Outline each Plasmodium malariae-infected red blood cell.
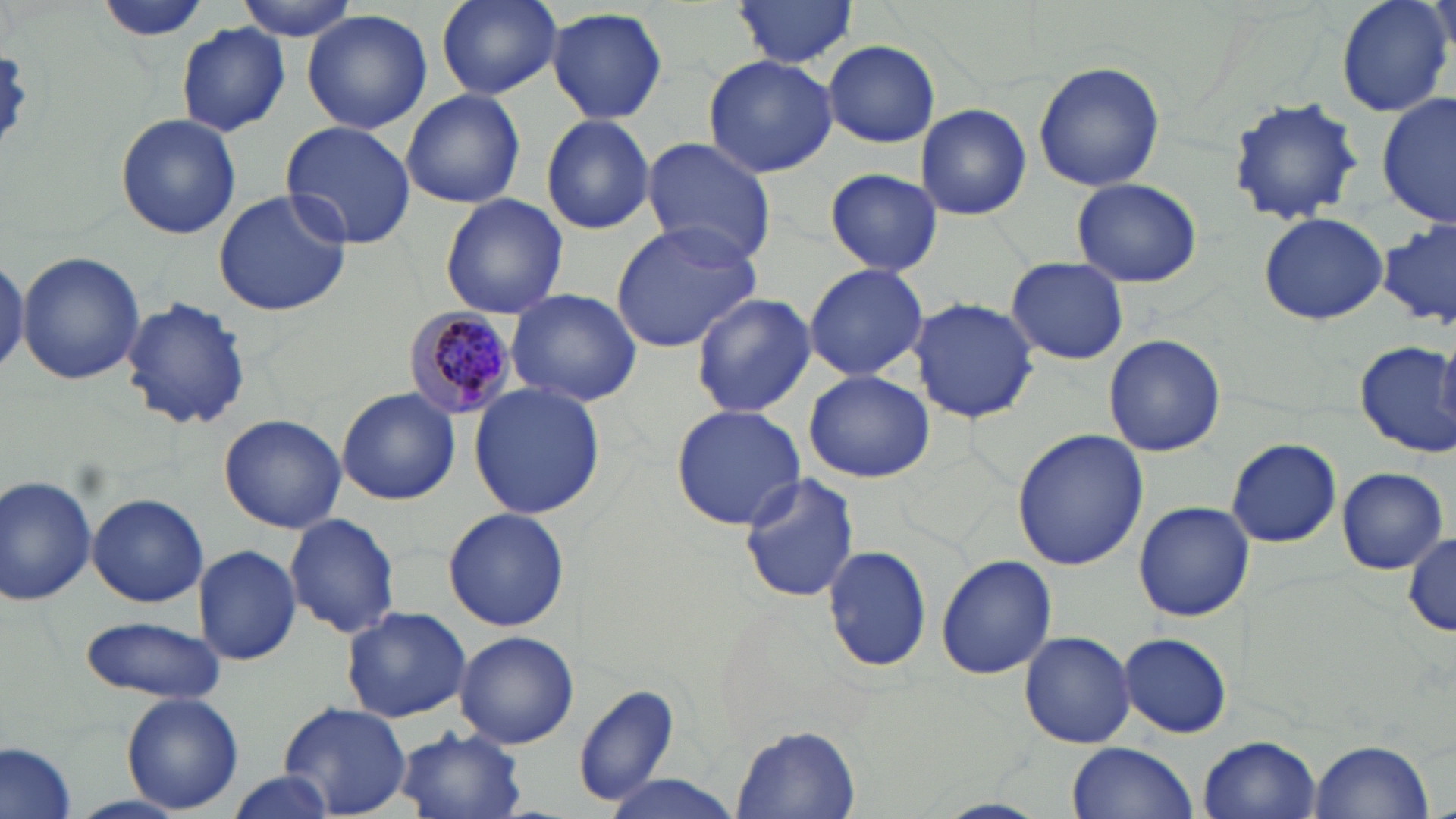

Approximate bounding boxes as named x1/y1/x2/y2 corners in pixels.
Plasmodium malariae-infected red blood cells: (x1=401, y1=304, x2=523, y2=419).

Summary:
  - Uninfected red blood cell locations: (x1=95, y1=0, x2=212, y2=46), (x1=237, y1=0, x2=363, y2=40), (x1=434, y1=0, x2=562, y2=100), (x1=732, y1=0, x2=860, y2=70), (x1=1334, y1=0, x2=1455, y2=119), (x1=547, y1=7, x2=668, y2=125), (x1=301, y1=9, x2=433, y2=135), (x1=176, y1=22, x2=292, y2=136), (x1=823, y1=40, x2=940, y2=147), (x1=701, y1=54, x2=839, y2=177), (x1=1033, y1=60, x2=1166, y2=192), (x1=400, y1=89, x2=525, y2=209), (x1=1378, y1=94, x2=1453, y2=227), (x1=1225, y1=97, x2=1367, y2=225), (x1=916, y1=104, x2=1031, y2=221), (x1=115, y1=113, x2=241, y2=240), (x1=540, y1=114, x2=657, y2=235), (x1=281, y1=120, x2=417, y2=248), (x1=640, y1=138, x2=776, y2=265), (x1=825, y1=167, x2=943, y2=275), (x1=1070, y1=177, x2=1204, y2=289), (x1=213, y1=188, x2=354, y2=317), (x1=439, y1=194, x2=567, y2=319), (x1=1258, y1=212, x2=1389, y2=325), (x1=608, y1=221, x2=764, y2=354), (x1=1376, y1=221, x2=1456, y2=330), (x1=17, y1=251, x2=146, y2=386), (x1=0, y1=253, x2=27, y2=377), (x1=1005, y1=257, x2=1130, y2=365), (x1=803, y1=263, x2=928, y2=383), (x1=505, y1=286, x2=645, y2=407), (x1=691, y1=293, x2=815, y2=420), (x1=120, y1=296, x2=254, y2=432), (x1=912, y1=298, x2=1038, y2=425), (x1=1104, y1=334, x2=1226, y2=458), (x1=1355, y1=340, x2=1455, y2=458), (x1=1437, y1=346, x2=1456, y2=427), (x1=803, y1=370, x2=933, y2=483), (x1=470, y1=384, x2=604, y2=521), (x1=335, y1=388, x2=461, y2=504), (x1=670, y1=405, x2=806, y2=531), (x1=219, y1=414, x2=346, y2=533), (x1=1012, y1=428, x2=1147, y2=571), (x1=1225, y1=438, x2=1342, y2=548), (x1=1335, y1=467, x2=1447, y2=574), (x1=738, y1=472, x2=861, y2=604), (x1=0, y1=474, x2=100, y2=608), (x1=87, y1=494, x2=208, y2=607), (x1=1134, y1=501, x2=1254, y2=621), (x1=127, y1=506, x2=290, y2=659), (x1=444, y1=506, x2=570, y2=631), (x1=284, y1=513, x2=401, y2=640), (x1=1404, y1=530, x2=1455, y2=638), (x1=822, y1=543, x2=933, y2=674), (x1=193, y1=545, x2=301, y2=666), (x1=935, y1=553, x2=1056, y2=680), (x1=340, y1=608, x2=473, y2=722), (x1=76, y1=613, x2=228, y2=704), (x1=1019, y1=630, x2=1137, y2=749), (x1=455, y1=631, x2=579, y2=749), (x1=1120, y1=632, x2=1232, y2=738), (x1=572, y1=683, x2=680, y2=807), (x1=121, y1=692, x2=244, y2=813), (x1=280, y1=701, x2=411, y2=816), (x1=732, y1=725, x2=862, y2=817), (x1=394, y1=726, x2=529, y2=819), (x1=1199, y1=735, x2=1322, y2=817), (x1=1309, y1=739, x2=1435, y2=819), (x1=0, y1=742, x2=78, y2=819), (x1=1067, y1=743, x2=1198, y2=819), (x1=222, y1=771, x2=341, y2=819), (x1=602, y1=776, x2=743, y2=817)
  - Slide-level diagnosis: Plasmodium malariae
  - Preparation: thin blood film
  - Image size: 1456×819 pixels
  - Modality: optical microscopy
  - Field of view: single
  - Magnification: 1000x
  - Stain: May-Grünwald-Giemsa